Point out each leukocyte.
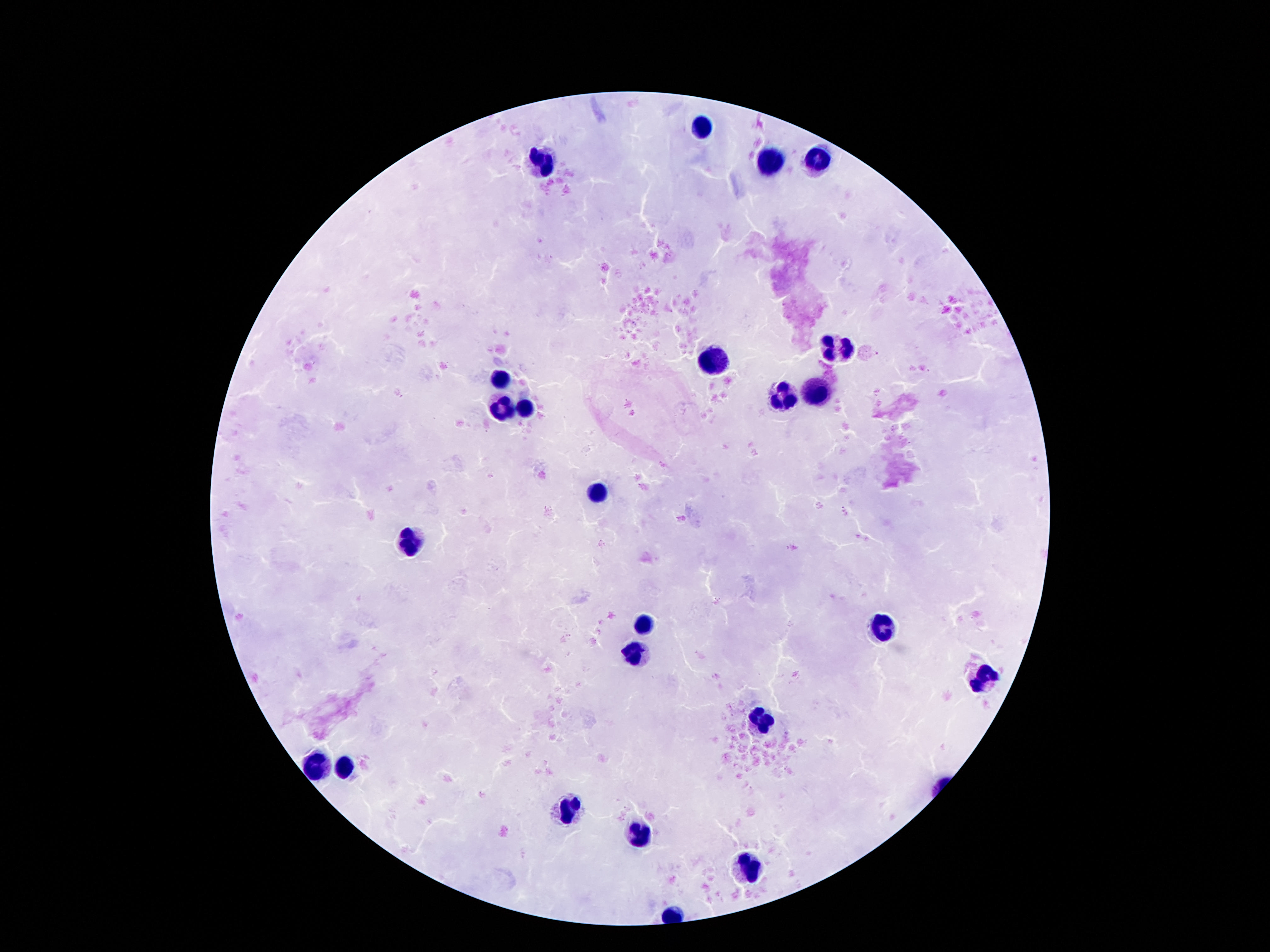
Approximate centers as {x, y} in pixels.
Leukocytes: {700, 124}, {821, 157}, {770, 161}, {540, 165}, {835, 348}, {712, 360}, {499, 376}, {815, 390}, {782, 401}, {524, 409}, {499, 413}, {594, 494}, {409, 544}, {645, 623}, {881, 629}, {635, 656}, {983, 680}, {762, 723}, {315, 764}, {344, 766}, {565, 809}, {637, 834}, {747, 867}.

Image is 1270×952 pixels. Giemsa stain. 100x magnification. One field from this slide. Patient malaria status: uninfected. Photographed through the microscope eyepiece with a smartphone camera. Thick blood smear.